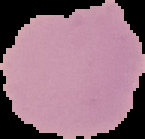

malaria status = uninfected
image type = cell region segmented out of the field of view; surrounding area masked to black
image size = 145×139 pixels
preparation = thin blood smear